Identify the blood parasite species.
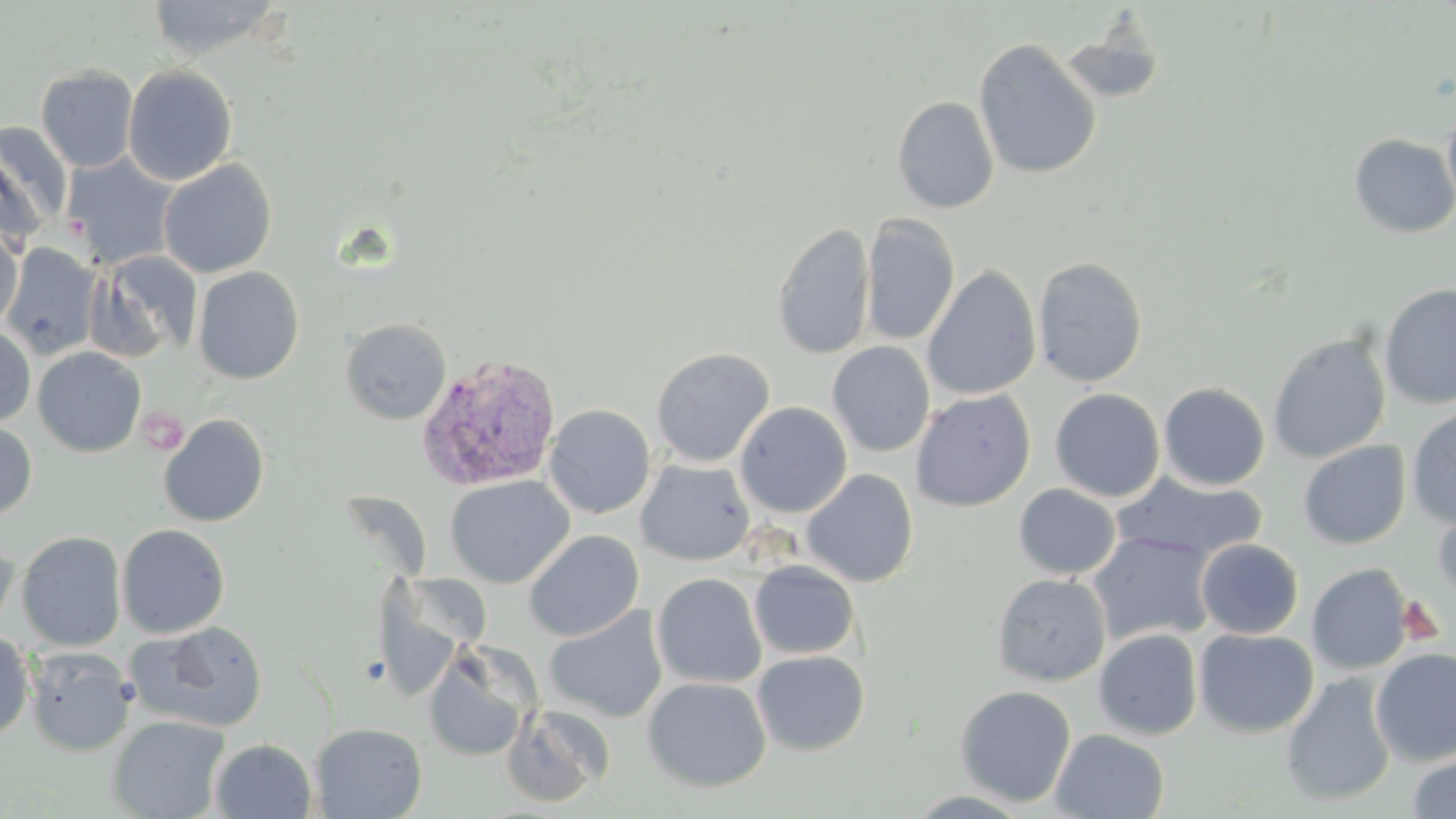

Plasmodium vivax.

Approximate bounding boxes as [x1, y1, x2, y2] in pixels. Uninfected red blood cell locations: [146, 0, 284, 60], [1059, 21, 1166, 106], [973, 37, 1102, 180], [36, 64, 139, 173], [122, 64, 237, 185], [892, 96, 1000, 214], [1442, 109, 1456, 212], [0, 125, 68, 242], [1349, 134, 1456, 239], [62, 154, 178, 268], [158, 158, 277, 278], [860, 214, 960, 347], [771, 221, 875, 360], [0, 225, 24, 330], [2, 243, 103, 360], [89, 250, 203, 363], [1032, 257, 1148, 387], [192, 266, 304, 384], [922, 266, 1041, 400], [1377, 283, 1456, 410], [340, 317, 452, 425], [0, 325, 36, 426], [1267, 333, 1391, 463], [827, 341, 935, 457], [33, 347, 146, 457], [651, 348, 774, 467], [1158, 382, 1270, 491], [1050, 388, 1165, 502], [911, 389, 1036, 512], [735, 402, 853, 517], [544, 404, 655, 519], [1405, 406, 1456, 529], [159, 413, 269, 527], [0, 421, 37, 522], [1299, 441, 1411, 549], [635, 459, 755, 565], [802, 468, 918, 588], [1112, 472, 1267, 563], [444, 475, 573, 589], [1014, 484, 1120, 579], [1432, 504, 1456, 607], [116, 524, 230, 637], [523, 529, 644, 642], [1087, 530, 1217, 646], [16, 531, 126, 651], [0, 533, 20, 637], [1195, 538, 1303, 639], [749, 560, 860, 659], [1307, 563, 1414, 675], [652, 572, 767, 689], [991, 573, 1112, 686], [544, 606, 668, 723], [130, 621, 270, 732], [1193, 627, 1318, 738], [1093, 628, 1203, 741], [0, 631, 35, 740], [423, 643, 537, 763], [25, 646, 136, 756], [1371, 648, 1456, 765], [752, 650, 870, 756], [1281, 671, 1397, 807], [642, 676, 772, 792], [954, 684, 1076, 807], [500, 703, 614, 808], [107, 714, 229, 819], [310, 722, 429, 818], [1050, 728, 1170, 819], [210, 738, 316, 818], [1405, 751, 1456, 819]. Platelet locations: [138, 405, 188, 455]. Plasmodium vivax-infected red blood cell locations: [416, 354, 562, 492]. One field of a larger specimen. 1000x magnification. May-Grünwald-Giemsa-stained preparation. Image is 1456×819 pixels. Thin blood film. Light microscopy.